Report the malaria status of this cell.
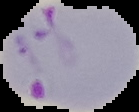
Parasitized.

From a thin blood film. Image is 139×112 pixels. Segmented cell region on a black background.